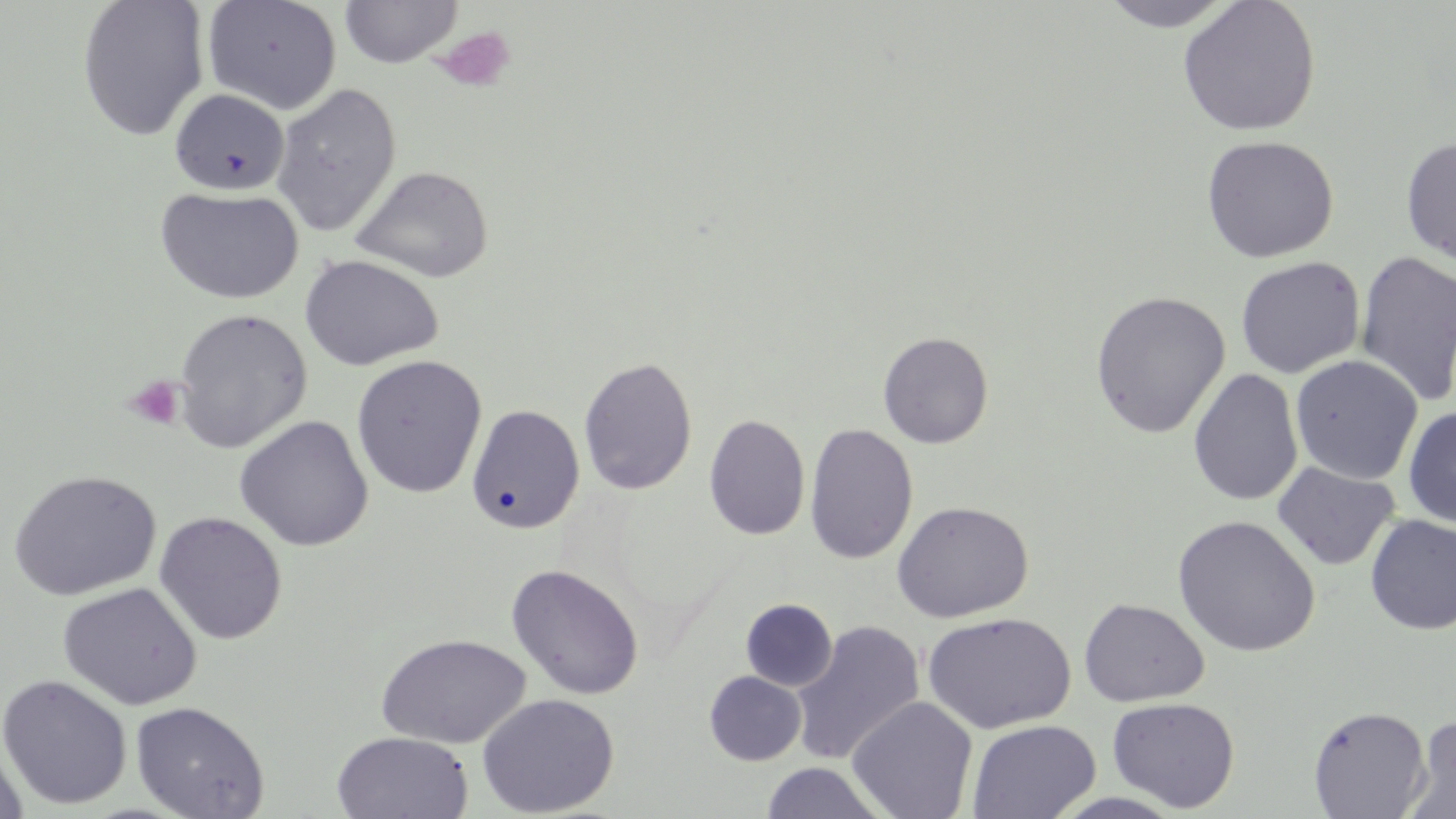
{
  "slide_level_diagnosis": "negative for blood parasites",
  "uninfected_red_blood_cell_locations": "approximate bounding boxes as (x1,y1)-(x2,y2) corner pairs in pixels: (76,0)-(210,141), (340,0)-(462,68), (1097,0)-(1238,31), (1177,0)-(1322,137), (202,1)-(342,115), (270,82)-(402,237), (168,88)-(290,196), (1201,134)-(1339,264), (1400,137)-(1456,267), (350,165)-(493,283), (154,185)-(304,305), (1354,250)-(1456,406), (299,254)-(444,371), (1235,257)-(1365,379), (1090,291)-(1231,438), (174,308)-(312,453), (878,331)-(994,449), (350,354)-(488,498), (1290,354)-(1423,485), (578,356)-(698,495), (1188,369)-(1304,506), (467,404)-(584,534), (1403,406)-(1456,528), (704,414)-(811,540), (233,415)-(374,552), (804,422)-(919,564), (1272,461)-(1400,571), (8,469)-(162,601), (892,501)-(1034,623), (153,511)-(288,645), (1365,514)-(1456,634), (1171,515)-(1320,657), (506,563)-(645,700), (57,582)-(202,711), (1079,598)-(1209,707), (740,599)-(838,692), (922,612)-(1076,734), (789,620)-(925,766), (375,633)-(531,749), (704,671)-(806,766), (0,674)-(133,810), (476,693)-(619,817), (847,696)-(978,819), (1107,697)-(1239,813), (130,700)-(270,819), (1307,705)-(1432,818), (1404,715)-(1456,818), (967,718)-(1101,819), (331,731)-(473,818), (0,736)-(29,819), (759,762)-(890,818), (1048,791)-(1188,818)",
  "stain": "May-Grünwald-Giemsa",
  "magnification": "1000x",
  "modality": "light microscopy",
  "image_size": "1456×819 pixels",
  "preparation": "thin blood smear",
  "field_of_view": "single",
  "platelet_locations": "approximate bounding boxes as (x1,y1)-(x2,y2) corner pairs in pixels: (433,26)-(517,93), (124,375)-(186,431)"
}